Describe the morphology of the red blood cells.
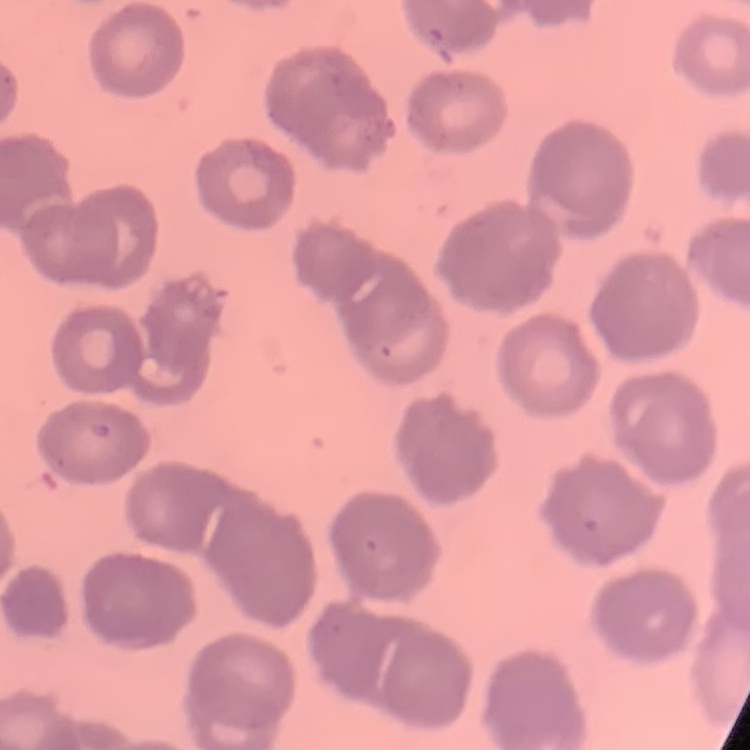

They show rouleaux formation.

preparation = thin peripheral smear
image type = square crop of a larger photomicrograph
stain = Field's or Giemsa